Identify the blood parasite species.
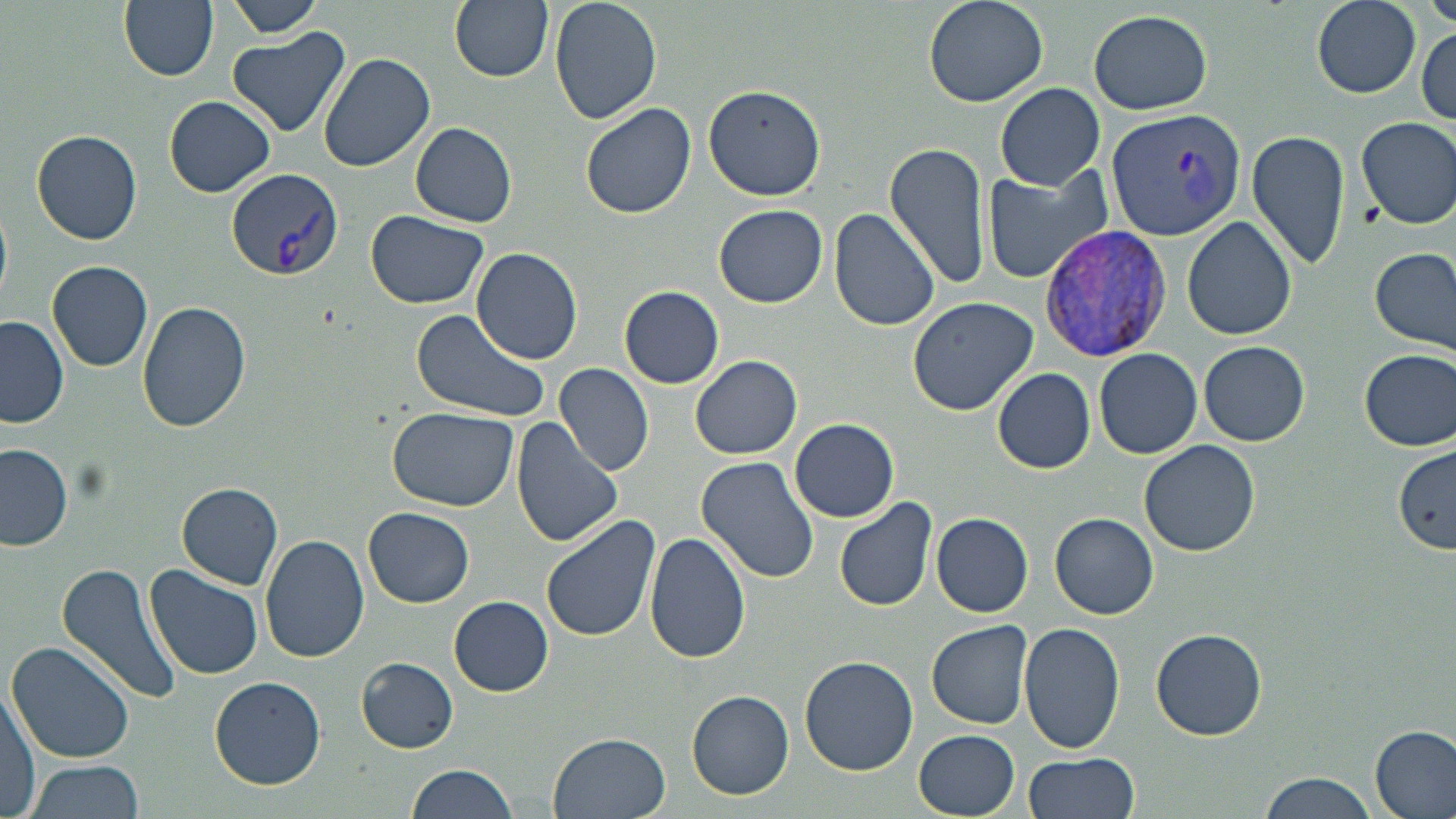

Plasmodium vivax.

Approximate bounding boxes as (x1,y1)-(x2,y2) corner pairs in pixels. Uninfected red blood cell locations: (119,0)-(219,81), (224,0)-(326,37), (449,0)-(554,81), (550,0)-(661,125), (922,0)-(1048,108), (1421,0)-(1456,33), (1313,1)-(1421,96), (1087,9)-(1213,116), (1414,24)-(1455,126), (224,28)-(352,138), (318,53)-(436,172), (702,83)-(827,202), (994,83)-(1103,190), (162,96)-(276,197), (581,101)-(696,219), (1355,115)-(1456,229), (409,121)-(517,228), (31,130)-(143,245), (1247,130)-(1351,270), (885,142)-(991,290), (983,166)-(1112,283), (714,204)-(828,308), (828,206)-(940,332), (366,210)-(491,309), (1182,215)-(1297,340), (1371,245)-(1456,356), (469,246)-(586,364), (47,260)-(153,372), (620,287)-(723,387), (906,295)-(1039,415), (137,300)-(252,431), (409,306)-(553,423), (0,316)-(68,428), (1199,341)-(1310,446), (1094,348)-(1203,459), (1360,349)-(1456,451), (690,356)-(802,459), (556,363)-(654,475), (992,367)-(1096,474), (385,406)-(518,511), (510,417)-(624,547), (789,418)-(899,523), (1139,438)-(1259,556), (1,443)-(74,551), (1393,445)-(1456,551), (694,456)-(819,583), (177,482)-(284,588), (834,498)-(938,613), (364,507)-(474,607), (932,512)-(1033,617), (1050,513)-(1158,617), (541,514)-(661,643), (644,532)-(751,665), (260,535)-(369,663), (56,563)-(184,708), (145,565)-(266,681), (449,597)-(552,694), (927,620)-(1034,729), (1019,621)-(1124,754), (1152,628)-(1267,741), (6,642)-(135,764), (800,655)-(918,775), (357,658)-(458,751), (209,675)-(326,789), (0,683)-(41,819), (687,691)-(793,798), (1372,725)-(1456,819), (915,730)-(1020,817), (549,731)-(672,819), (1023,752)-(1140,819), (24,759)-(146,817), (402,764)-(519,819), (1258,772)-(1377,819). Plasmodium vivax-infected red blood cell locations: (1107,109)-(1247,243), (226,167)-(344,280), (1038,224)-(1175,363). Thin blood film. Optical microscopy. May-Grünwald-Giemsa-stained preparation. Captured at 1000x magnification. One field of a larger specimen. Image is 1456×819 pixels.